Identify the parasite.
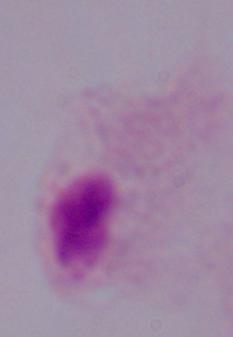
A trichomonad.

1000x magnification. Photomicrograph.